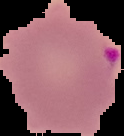
Image is 124×136 pixels. Malaria status: parasitized. From a thin blood smear. Cell region segmented out of the field of view; the surrounding area is masked to black.